Assess this cell for malaria.
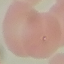

It is parasitized.

Thin blood smear. Cell patch, automatically extracted from a larger field of view and resized to 64 × 64 pixels. Acquired by smartphone through the microscope eyepiece. Giemsa stain.